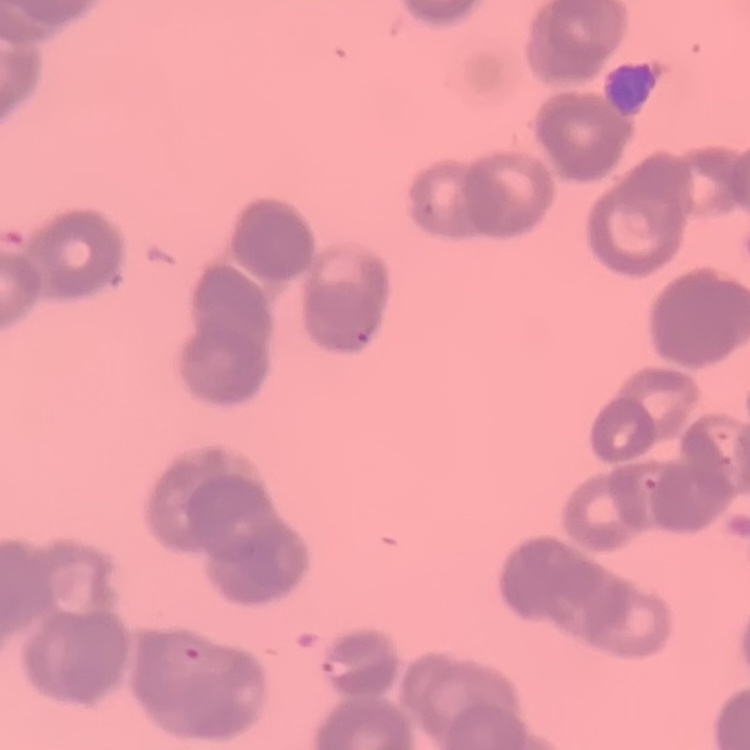

Summary:
  - Erythrocyte morphology: rouleaux formation
  - Preparation: thin peripheral smear
  - Image type: one tile cut from a larger photomicrograph
  - Stain: Field's or Giemsa